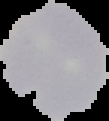

Result: no Plasmodium parasites seen. The area outside the segmented cell region is set to black. Image is 109×121 pixels. From a thin blood film.